Classify this cell by malaria status.
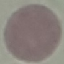
It is uninfected.

Summary:
  - Stain: Giemsa
  - Image type: automatically extracted cell patch, resized to 64 × 64 pixels
  - Capture: smartphone through the microscope eyepiece
  - Preparation: thin blood smear